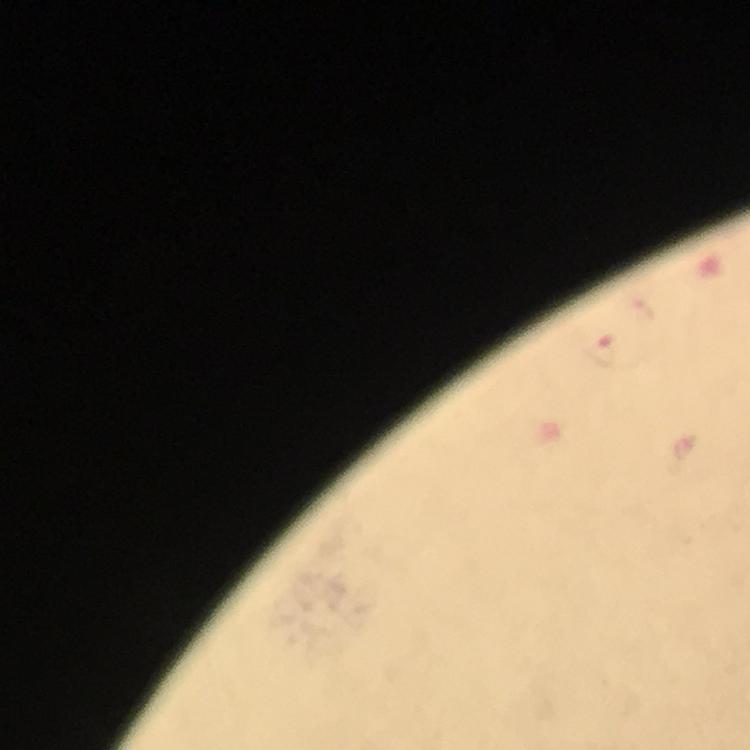

Approximate centers as {x, y} in pixels. Plasmodium parasite locations: {600, 348}. Giemsa stain. From a malaria diagnostic workup. 100x magnification. Immersion oil applied. Image is 750×750 pixels. Photographed with a smartphone mounted on the microscope. Thick blood smear. Cropped region of a single field of view.